Name the parasite shown.
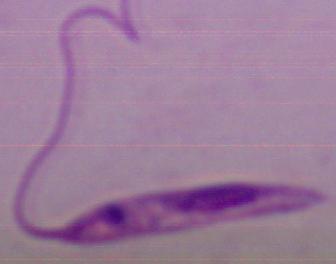
This is Leishmania.

Summary:
  - Magnification: 1000x
  - Modality: photomicrograph